Locate and identify every blood parasite.
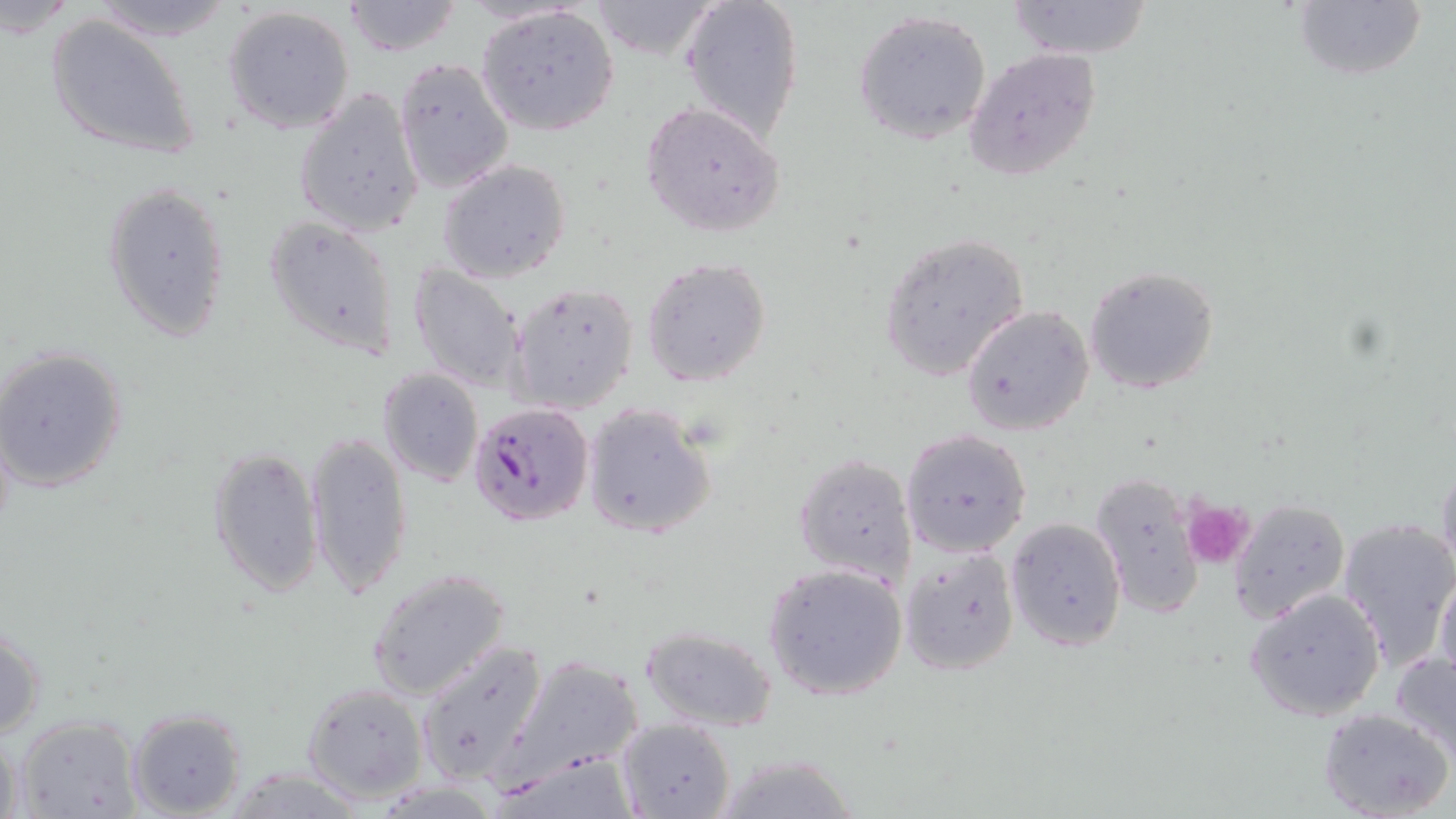
Approximate bounding boxes as (x1,y1)-(x2,y2) corner pairs in pixels.
Plasmodium falciparum-infected red blood cells: (468,401)-(593,527).
No Plasmodium ovale, Plasmodium malariae, Plasmodium vivax, Babesia divergens, or Trypanosoma brucei observed.

{
  "slide_level_diagnosis": "Plasmodium falciparum",
  "image_size": "1456×819 pixels",
  "platelet_locations": "approximate bounding boxes as (x1,y1)-(x2,y2) corner pairs in pixels: (1180,498)-(1255,570)",
  "modality": "light microscopy",
  "uninfected_red_blood_cell_locations": "approximate bounding boxes as (x1,y1)-(x2,y2) corner pairs in pixels: (88,0)-(234,40), (585,0)-(719,63), (681,0)-(804,142), (1291,0)-(1427,84), (341,1)-(465,57), (1006,1)-(1155,61), (223,5)-(356,134), (475,5)-(620,135), (852,8)-(992,144), (46,15)-(198,160), (962,47)-(1103,183), (393,58)-(514,195), (292,87)-(425,236), (641,100)-(787,238), (437,159)-(572,282), (103,181)-(231,341), (263,216)-(403,360), (878,233)-(1030,382), (642,257)-(772,390), (408,262)-(526,393), (1083,265)-(1221,395), (507,282)-(638,413), (961,305)-(1095,435), (0,346)-(128,493), (377,368)-(484,487), (580,402)-(717,539), (900,428)-(1033,558), (304,430)-(413,599), (206,446)-(323,598), (794,453)-(916,586), (1435,459)-(1456,585), (1088,470)-(1206,617), (1227,498)-(1352,623), (1005,516)-(1126,650), (1335,517)-(1456,672), (900,545)-(1021,675), (762,562)-(909,701), (1434,563)-(1456,686), (367,569)-(512,701), (1244,586)-(1387,723), (0,622)-(45,745), (640,626)-(777,732), (413,640)-(551,787), (1390,649)-(1456,758), (502,657)-(643,780), (301,683)-(428,804), (1319,706)-(1454,819), (128,708)-(244,818), (12,714)-(143,819), (616,717)-(735,819), (0,735)-(25,819), (709,752)-(862,819)",
  "stain": "May-Grünwald-Giemsa",
  "field_of_view": "one of a larger specimen",
  "preparation": "thin blood film",
  "magnification": "1000x"
}